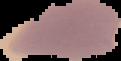
Summary:
  - Preparation: thin blood smear
  - Image size: 121×61 pixels
  - Image type: cell region segmented out of the field of view; surrounding area masked to black
  - Result: Plasmodium parasites detected